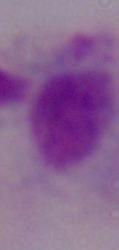
modality = micrograph
magnification = 1000x
identification = trichomonad